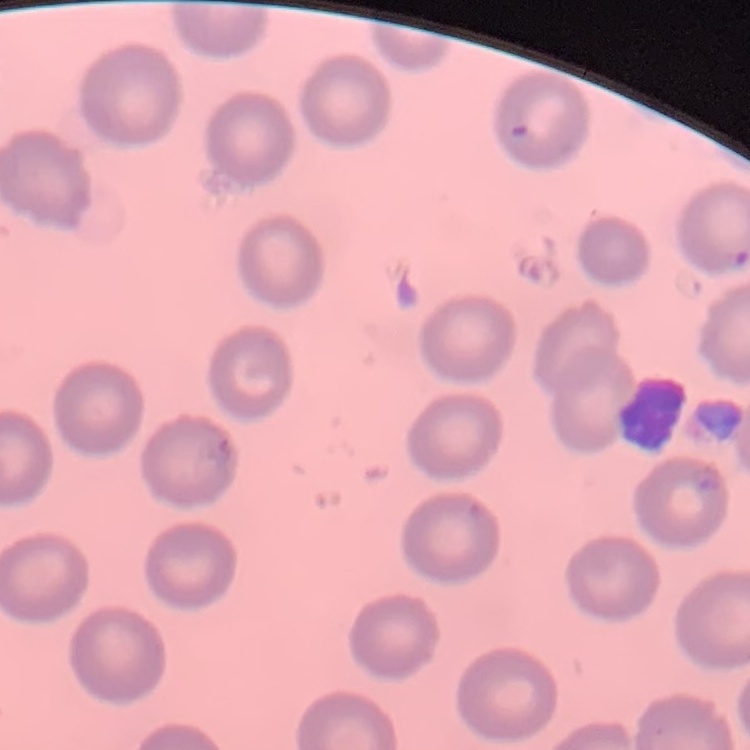

Summary:
  - Red blood cell morphology: no rouleaux formation
  - Preparation: thin peripheral smear
  - Image type: one tile cut from a larger photomicrograph
  - Stain: Field's or Giemsa